Give the position of every Plasmodium parasite visible.
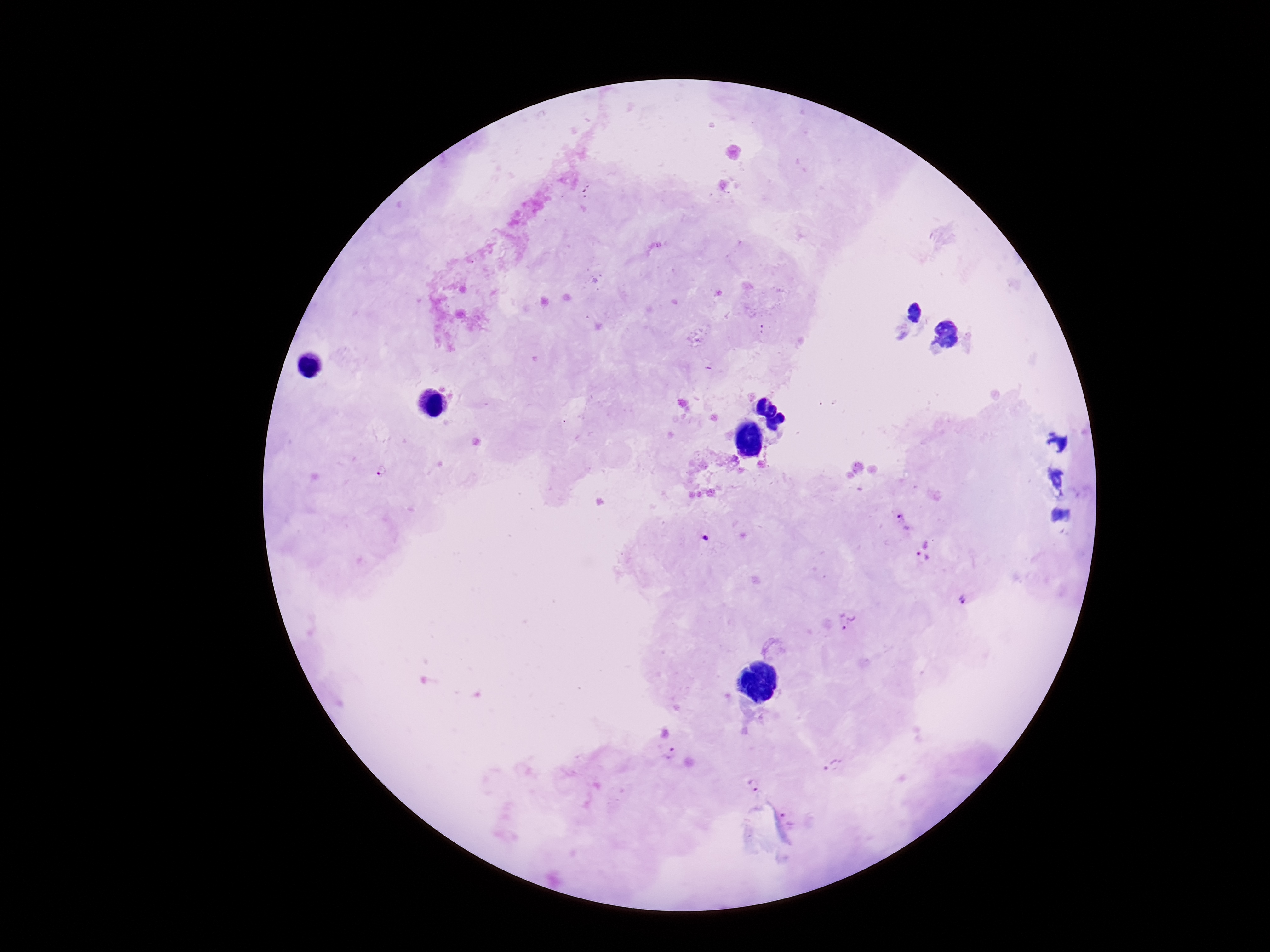
Approximate centers as [x, y] in pixels.
Plasmodium parasites: [764, 331], [384, 472], [903, 522], [707, 539], [926, 550], [964, 600], [847, 622], [669, 754], [834, 765], [755, 785], [787, 819].

Patient malaria status: positive. Image is 1270×952 pixels. Thick blood smear. 100x magnification. Giemsa stain. One field from this slide. Photographed through the microscope eyepiece with a smartphone camera.